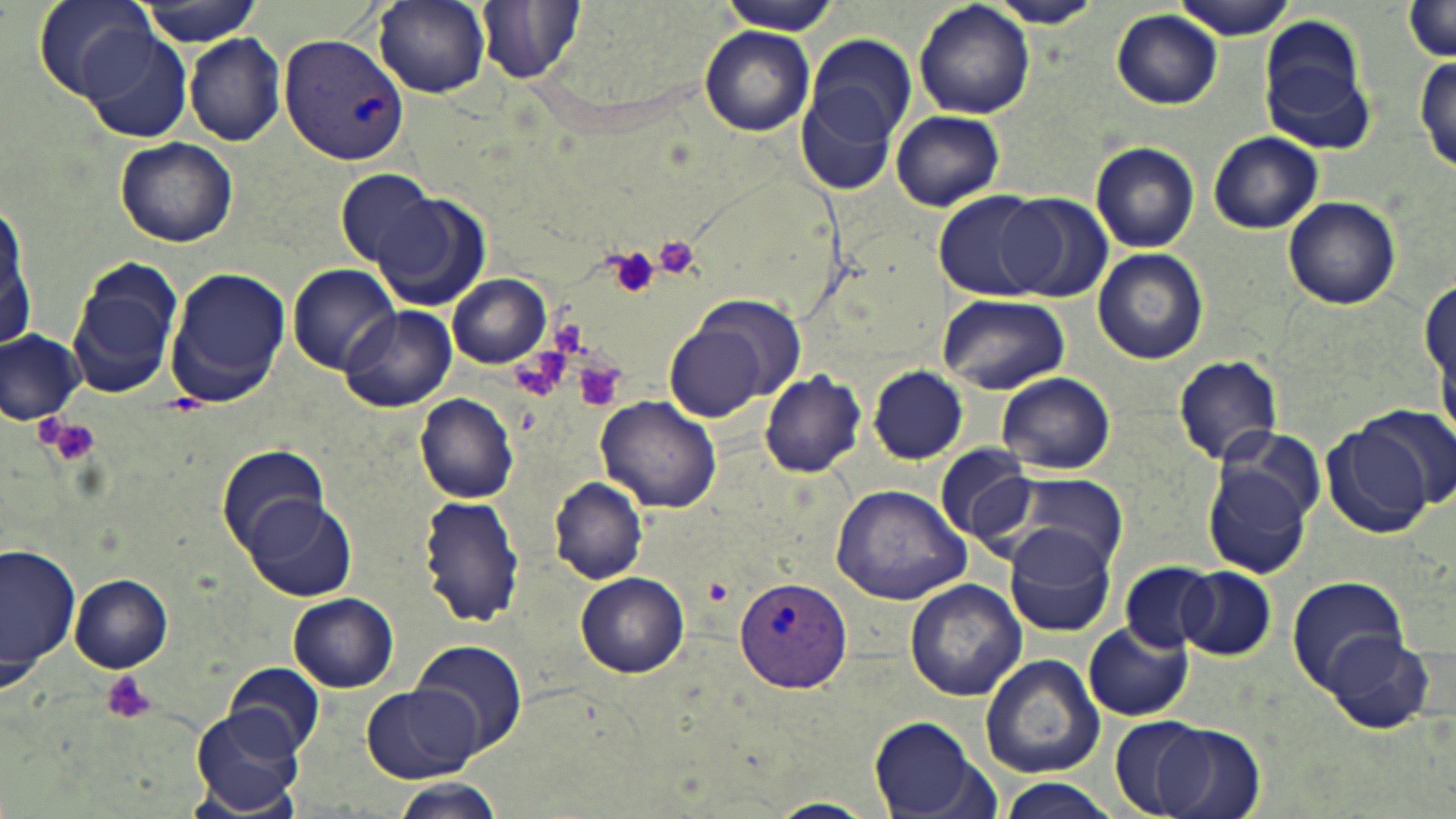
slide-level diagnosis = Plasmodium vivax
modality = optical microscopy
preparation = thin blood smear
image size = 1456×819 pixels
uninfected red blood cell locations = approximate bounding boxes as (x1, y1, x2, y2) in pixels: (31, 0, 162, 101), (131, 0, 265, 46), (373, 0, 490, 96), (1175, 0, 1295, 39), (476, 1, 586, 83), (914, 1, 1035, 118), (992, 1, 1100, 28), (718, 2, 840, 34), (1399, 3, 1456, 67), (1111, 8, 1223, 110), (1258, 24, 1375, 151), (699, 27, 814, 137), (81, 28, 192, 144), (184, 32, 286, 146), (809, 34, 917, 149), (1415, 54, 1455, 175), (795, 73, 906, 199), (888, 107, 1007, 212), (1209, 132, 1323, 233), (115, 136, 238, 247), (1090, 141, 1199, 252), (332, 167, 442, 272), (935, 191, 1053, 300), (371, 192, 491, 313), (0, 193, 29, 357), (999, 193, 1113, 304), (1283, 195, 1400, 311), (1093, 248, 1209, 365), (68, 260, 182, 401), (287, 264, 401, 374), (164, 267, 290, 406), (448, 274, 551, 368), (937, 294, 1069, 394), (691, 296, 806, 401), (341, 305, 456, 413), (665, 324, 768, 421), (0, 330, 85, 426), (1173, 354, 1283, 466), (867, 365, 969, 464), (759, 370, 865, 478), (996, 373, 1117, 474), (415, 393, 518, 503), (595, 397, 721, 513), (1360, 403, 1454, 511), (1324, 423, 1437, 537), (216, 444, 332, 554), (935, 444, 1038, 547), (1203, 447, 1319, 580), (984, 473, 1132, 571), (548, 477, 649, 585), (830, 482, 974, 606), (419, 493, 524, 628), (238, 495, 358, 603), (1004, 525, 1120, 639), (2, 540, 78, 691), (0, 550, 157, 677), (1119, 561, 1216, 652), (1176, 565, 1276, 660), (575, 573, 690, 678), (1285, 574, 1413, 695), (70, 575, 174, 671), (905, 579, 1028, 701), (288, 592, 399, 690), (1083, 623, 1192, 721), (1322, 631, 1438, 735), (410, 639, 526, 755), (979, 652, 1104, 778), (225, 661, 323, 759), (362, 685, 481, 782), (191, 709, 303, 816), (1108, 716, 1209, 818), (869, 717, 994, 817), (1153, 723, 1265, 819), (995, 778, 1123, 819), (385, 779, 509, 818), (765, 799, 881, 818)
Plasmodium vivax-infected red blood cell locations = approximate bounding boxes as (x1, y1, x2, y2) in pixels: (279, 33, 407, 165), (734, 575, 853, 693)
field of view = single
magnification = 1000x
platelet locations = approximate bounding boxes as (x1, y1, x2, y2) in pixels: (653, 235, 703, 279), (604, 244, 662, 303), (576, 361, 628, 413), (44, 418, 100, 466), (101, 671, 159, 724)
stain = May-Grünwald-Giemsa